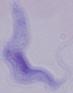

A trypanosome is seen. 1000x magnification. Photomicrograph.